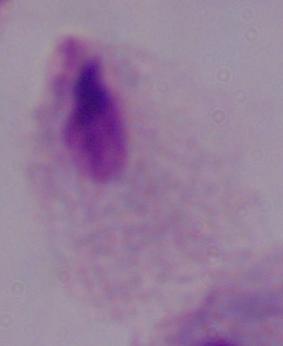
Summary:
  - Modality: micrograph
  - Identification: trichomonad
  - Magnification: 1000x